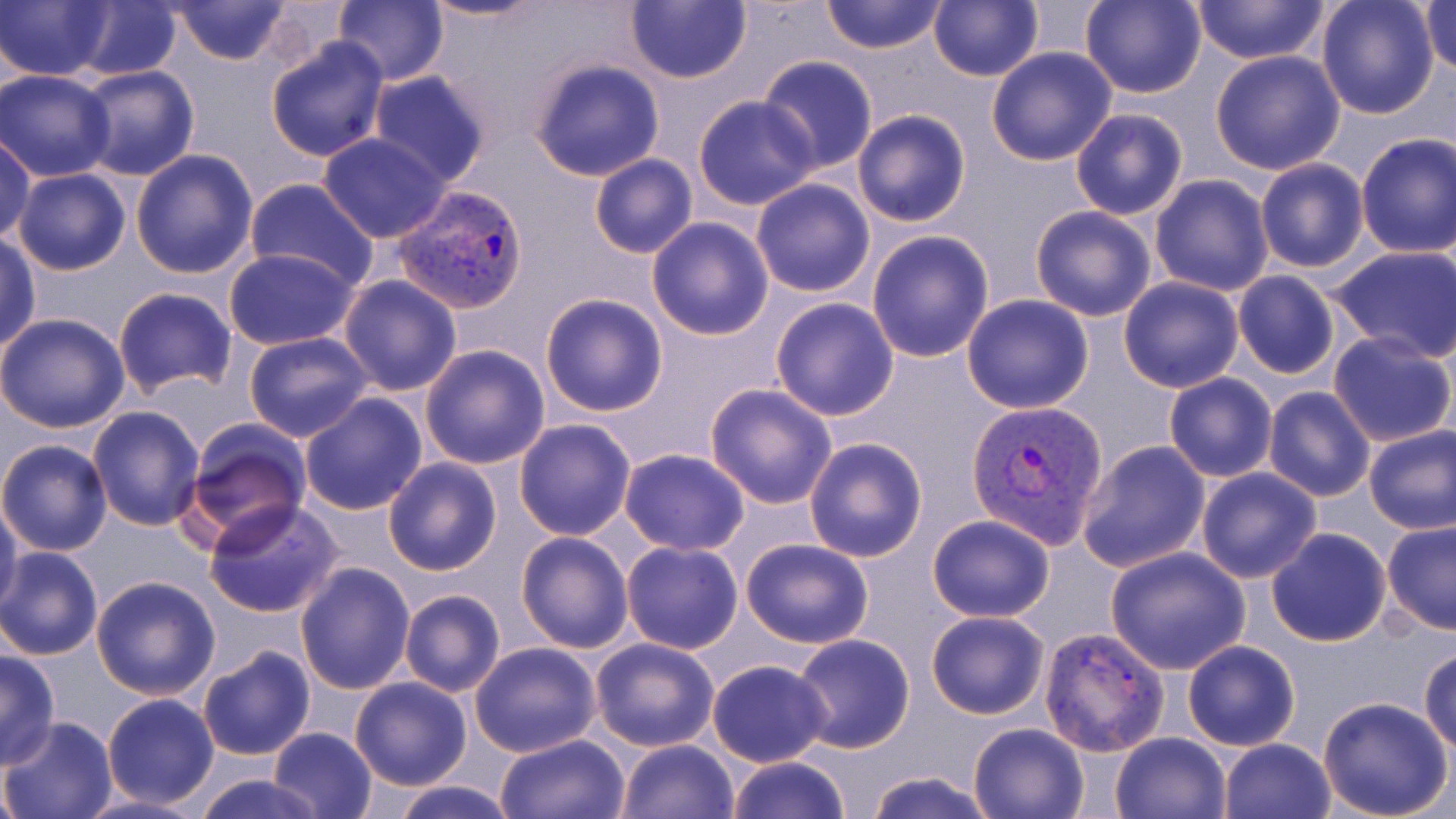
slide-level diagnosis = Plasmodium vivax
magnification = 1000x
stain = May-Grünwald-Giemsa
modality = light microscopy
Plasmodium vivax-infected red blood cell locations = approximate bounding boxes as [x1, y1, x2, y2] in pixels: [393, 184, 529, 315], [966, 399, 1110, 548], [1038, 626, 1170, 756]
image size = 1456×819 pixels
uninfected red blood cell locations = approximate bounding boxes as [x1, y1, x2, y2] in pixels: [2, 0, 115, 82], [169, 0, 293, 66], [333, 0, 449, 85], [420, 0, 554, 24], [624, 0, 750, 85], [820, 0, 947, 54], [929, 0, 1043, 82], [1080, 0, 1206, 99], [1192, 0, 1329, 67], [1315, 0, 1440, 119], [1422, 0, 1455, 77], [65, 1, 182, 80], [266, 38, 390, 163], [986, 47, 1117, 166], [1208, 49, 1348, 174], [757, 56, 878, 175], [527, 58, 666, 181], [75, 66, 200, 182], [1, 70, 118, 181], [366, 70, 491, 186], [693, 94, 820, 210], [1070, 108, 1190, 221], [851, 109, 972, 227], [317, 132, 452, 242], [1354, 133, 1456, 257], [0, 135, 34, 247], [131, 149, 260, 279], [587, 154, 698, 259], [1255, 158, 1370, 274], [13, 170, 130, 276], [1149, 174, 1275, 296], [244, 177, 378, 289], [750, 178, 875, 297], [1029, 204, 1157, 322], [647, 217, 774, 340], [866, 229, 995, 362], [0, 234, 41, 352], [1328, 245, 1456, 364], [223, 247, 359, 350], [1232, 270, 1342, 378], [338, 274, 463, 396], [1118, 277, 1245, 393], [112, 287, 238, 398], [540, 293, 669, 418], [961, 295, 1093, 413], [770, 296, 900, 421], [0, 312, 129, 433], [1328, 331, 1456, 446], [244, 332, 372, 442], [419, 344, 550, 469], [1164, 372, 1278, 482], [704, 382, 838, 510], [1262, 385, 1377, 501], [299, 392, 429, 515], [86, 404, 206, 531], [513, 418, 636, 540], [180, 423, 311, 552], [1363, 426, 1456, 535], [804, 435, 928, 561], [0, 438, 112, 556], [1076, 440, 1210, 574], [619, 448, 751, 556], [383, 457, 504, 576], [1195, 468, 1321, 583], [1, 497, 23, 612], [204, 497, 345, 618], [925, 514, 1056, 621], [1381, 521, 1456, 636], [1265, 528, 1392, 648], [515, 531, 635, 654], [739, 539, 876, 649], [621, 540, 744, 654], [0, 546, 103, 659], [1105, 547, 1251, 674], [294, 561, 416, 695], [91, 575, 221, 700], [398, 589, 505, 696], [926, 611, 1050, 719], [790, 634, 916, 754], [589, 637, 722, 752], [1182, 639, 1301, 751], [468, 641, 601, 757], [196, 645, 317, 760], [1420, 650, 1456, 752], [0, 651, 60, 768], [705, 659, 835, 768], [348, 676, 473, 790], [100, 693, 219, 809], [1318, 697, 1453, 819], [1, 717, 119, 819], [967, 720, 1092, 818], [267, 727, 378, 819], [1110, 731, 1232, 819], [496, 733, 628, 818], [1219, 738, 1337, 819], [615, 739, 739, 819], [724, 755, 853, 818], [196, 771, 325, 819], [866, 771, 993, 819], [387, 780, 519, 819], [69, 792, 213, 819]
field of view = one of a larger specimen
preparation = thin blood film